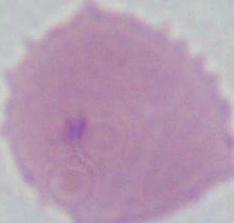

Summary:
  - Modality: micrograph
  - Magnification: 1000x
  - Identification: erythrocyte